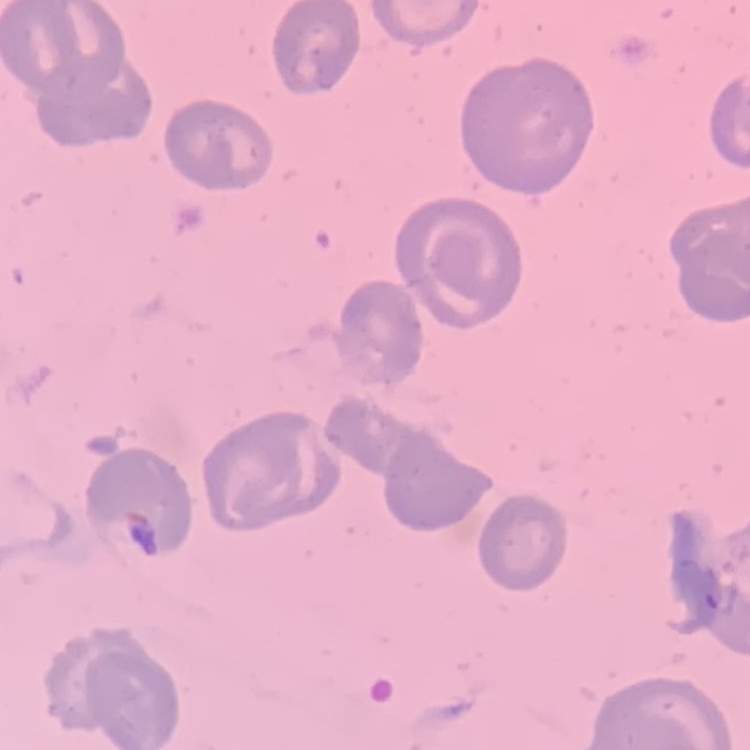

Summary:
  - Erythrocyte morphology: no rouleaux formation
  - Image type: one tile cut from a larger photomicrograph
  - Preparation: thin peripheral smear
  - Stain: Field's or Giemsa